Classify this cell by malaria status.
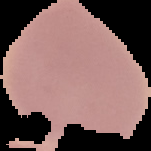

It is uninfected.

Summary:
  - Image size: 151×151 pixels
  - Image type: segmented cell region with the area outside set to black
  - Preparation: thin blood film